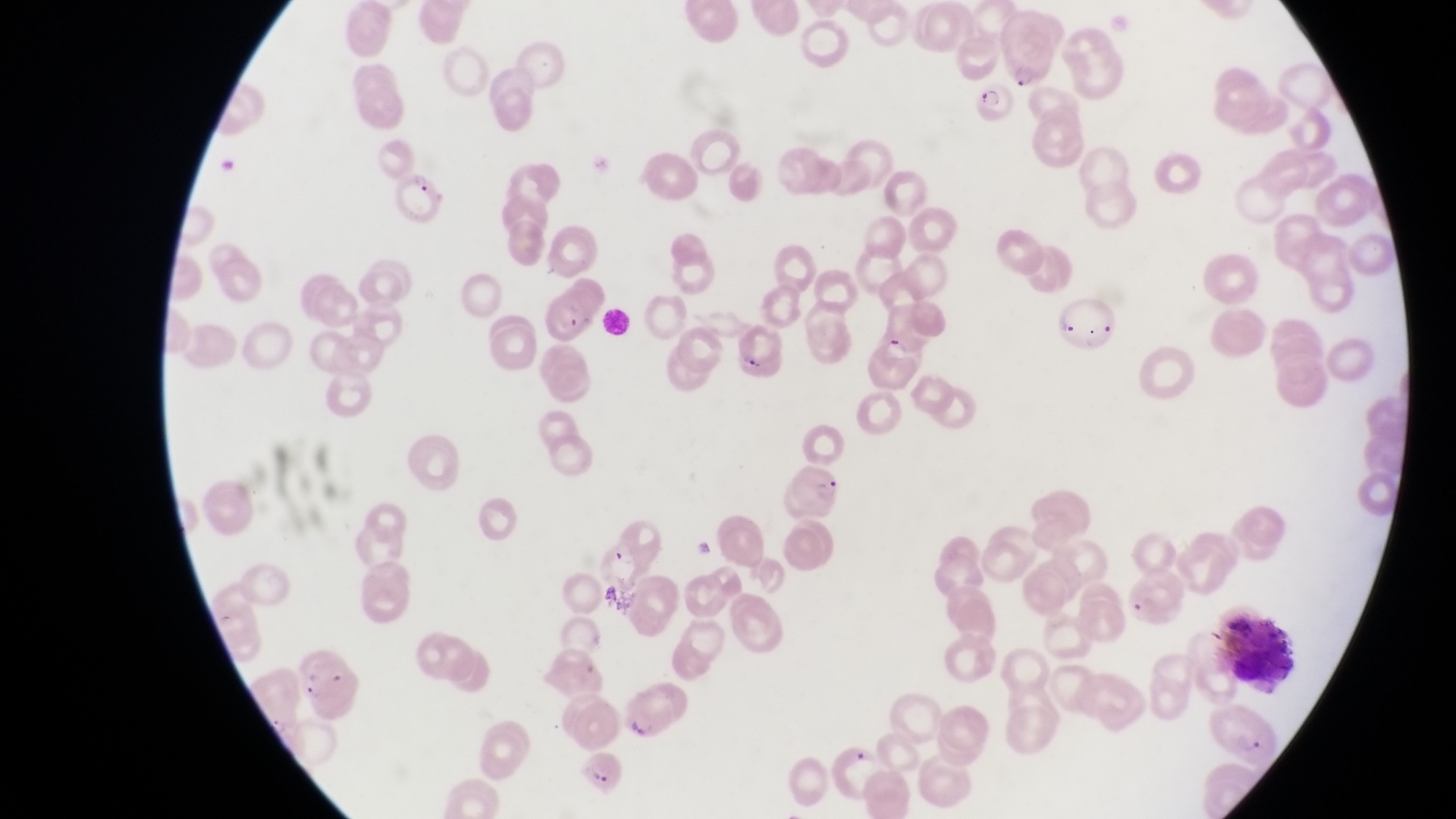
Approximate bounding boxes as [left, top, right, bottom] in pixels.
Summary:
  - Leukocyte locations: [1213, 608, 1298, 688]
  - Parasitised red blood cell locations: [1010, 29, 1060, 88], [971, 76, 1018, 125], [386, 162, 447, 215], [542, 296, 591, 355], [1054, 297, 1117, 350], [732, 327, 785, 383], [614, 686, 670, 744], [578, 753, 631, 798]
  - Country: Uganda
  - Capture: smartphone photograph through the eyepiece of an Olympus CX-23 microscope
  - Field of view: single
  - Preparation: thin blood film
  - Image size: 1456×819 pixels
  - Magnification: 1000x